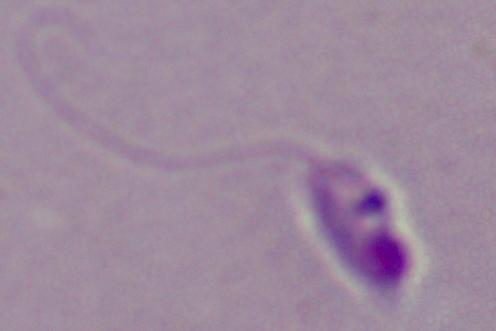

Summary:
  - Identification: Leishmania
  - Modality: photomicrograph
  - Magnification: 1000x